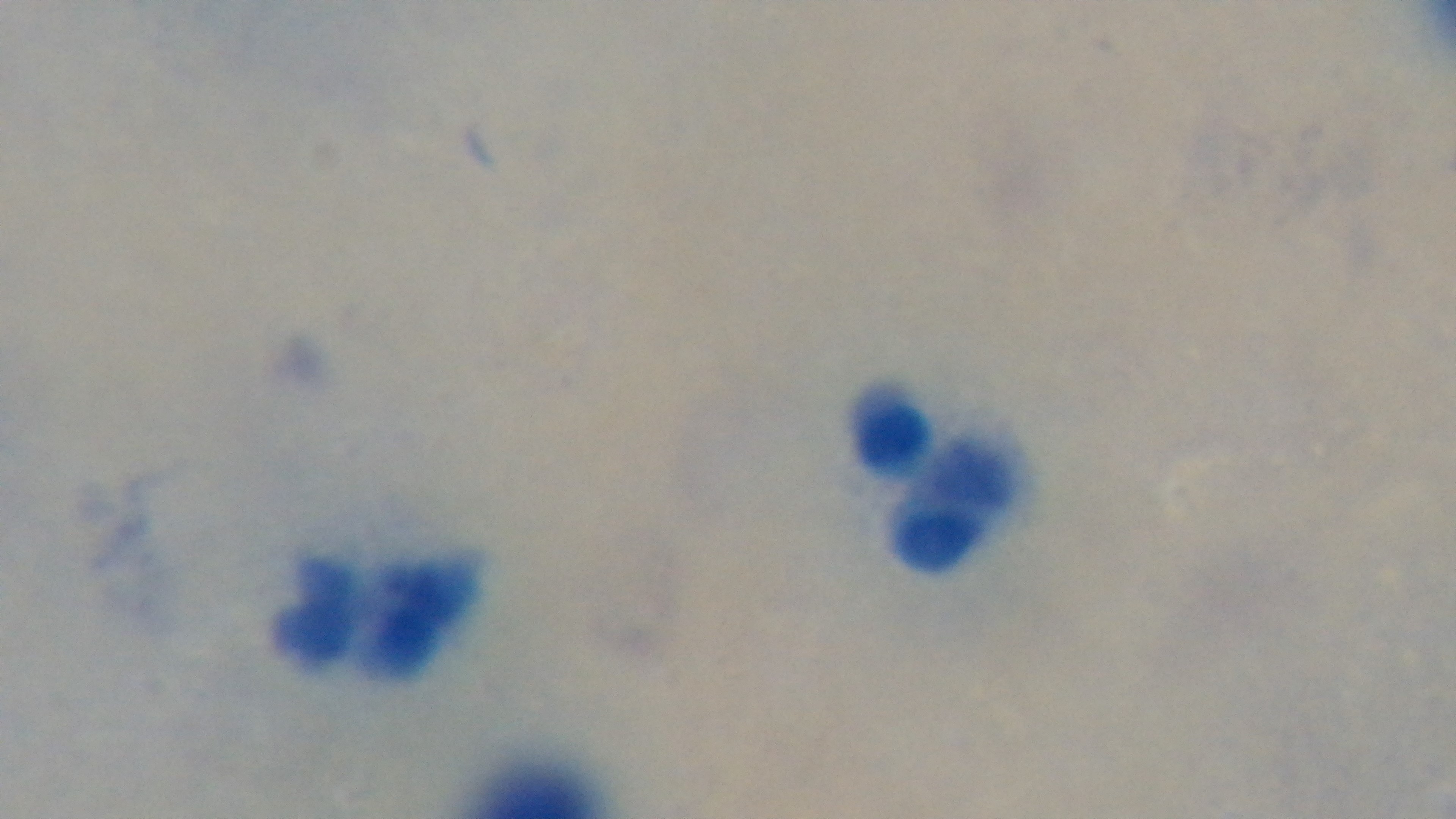
objective: 100x oil immersion
preparation: thick blood film
malaria_status: negative
capture: mounted 4K digital camera
field_of_view: single
stain: Giemsa
modality: light microscopy